Outline each blood parasite and name the species.
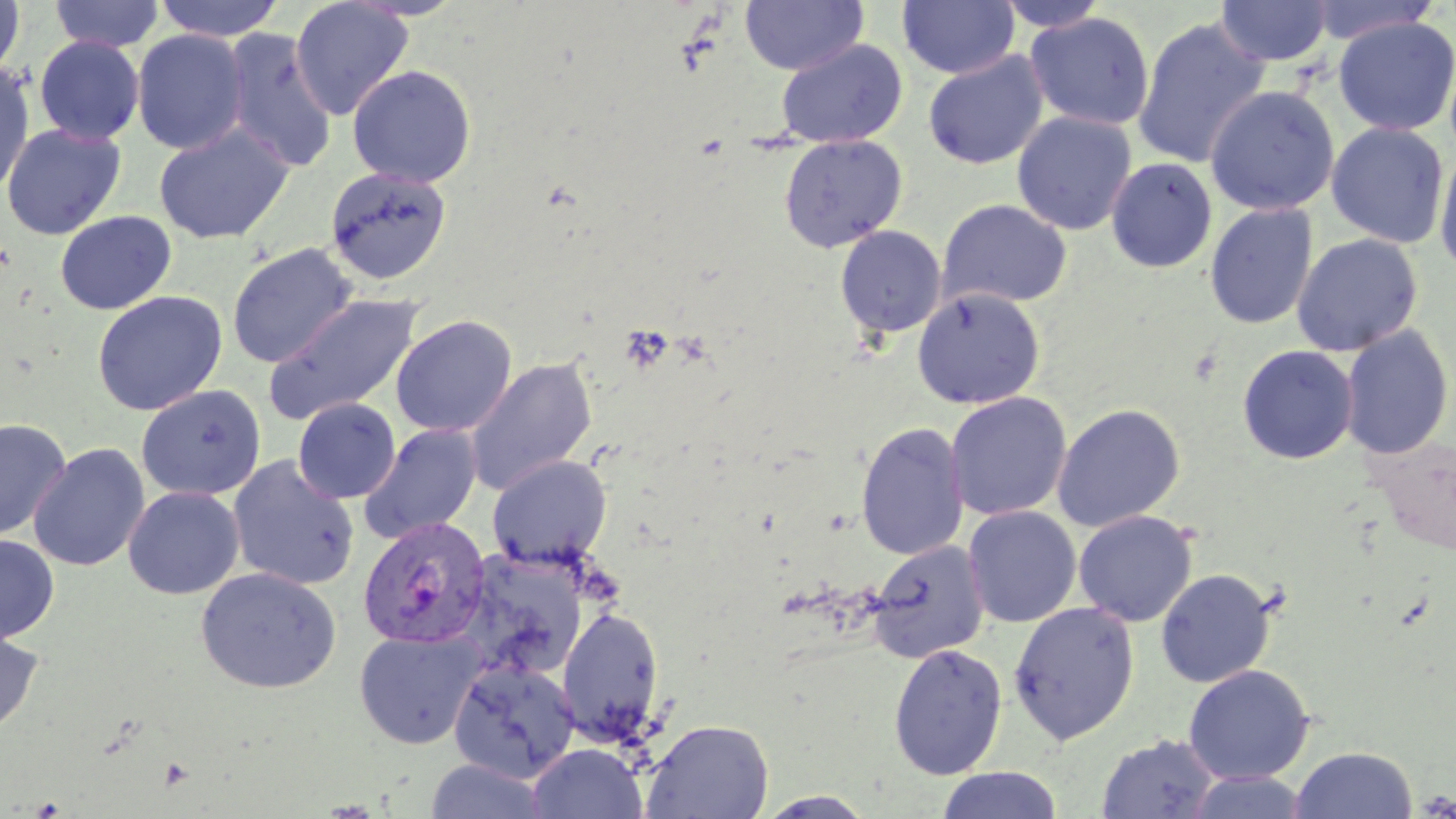

Approximate bounding boxes as (x1, y1, x2, y2) in pixels.
Plasmodium vivax-infected red blood cells: (359, 517, 496, 650).
No Plasmodium falciparum, Plasmodium ovale, Plasmodium malariae, Babesia divergens, or Trypanosoma brucei observed.

Uninfected red blood cell locations: (0, 0, 25, 83), (49, 0, 163, 52), (153, 0, 286, 42), (290, 0, 413, 119), (740, 0, 867, 75), (898, 0, 1019, 80), (1303, 0, 1443, 45), (994, 1, 1111, 32), (1216, 1, 1332, 66), (1024, 12, 1155, 131), (1132, 16, 1270, 169), (1333, 16, 1456, 136), (131, 30, 248, 154), (222, 30, 337, 173), (34, 36, 144, 145), (775, 38, 907, 147), (923, 51, 1049, 169), (1, 63, 35, 195), (347, 65, 477, 188), (1204, 85, 1340, 215), (1011, 111, 1137, 235), (154, 122, 294, 244), (1326, 122, 1450, 249), (1, 123, 126, 240), (778, 135, 908, 254), (1434, 144, 1456, 274), (1105, 157, 1218, 273), (324, 167, 452, 285), (936, 198, 1072, 309), (1204, 202, 1318, 330), (55, 211, 176, 314), (834, 225, 947, 337), (1291, 233, 1423, 356), (227, 243, 356, 369), (911, 287, 1046, 409), (92, 290, 228, 416), (263, 293, 423, 424), (391, 315, 517, 437), (1339, 324, 1454, 460), (1237, 344, 1359, 465), (465, 356, 598, 496), (136, 384, 265, 501), (945, 391, 1071, 521), (293, 398, 401, 503), (1052, 402, 1186, 532), (0, 418, 72, 541), (856, 420, 969, 561), (360, 424, 483, 544), (28, 442, 149, 572), (487, 454, 612, 570), (227, 456, 360, 591), (123, 486, 244, 599), (963, 506, 1082, 628), (1073, 510, 1198, 627), (0, 535, 59, 643), (866, 538, 989, 663), (455, 551, 589, 683), (195, 567, 341, 693), (1155, 568, 1277, 688), (1008, 601, 1140, 745), (556, 605, 665, 745), (0, 627, 43, 738), (354, 627, 485, 749), (888, 642, 1008, 779), (449, 658, 581, 784), (1183, 663, 1315, 784), (640, 718, 774, 819), (1096, 733, 1221, 818), (527, 743, 648, 818), (1290, 746, 1418, 819), (422, 759, 553, 819), (935, 767, 1064, 818), (1183, 771, 1310, 819), (754, 790, 879, 818). Slide-level diagnosis: Plasmodium vivax. 1000x magnification. Optical microscopy. May-Grünwald-Giemsa stain. Image is 1456×819 pixels. One field of a larger specimen. Thin blood smear.